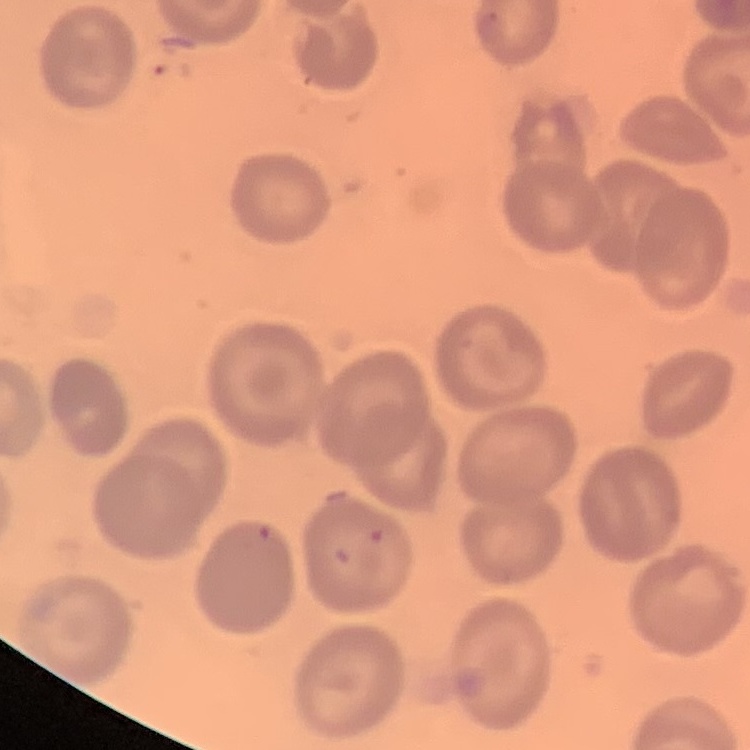 The erythrocytes show no rouleaux formation. Thin blood smear. Stained with either Field's or Giemsa. Square crop of a larger photomicrograph.